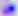
identification = Toxoplasma gondii
modality = photomicrograph
magnification = 400x